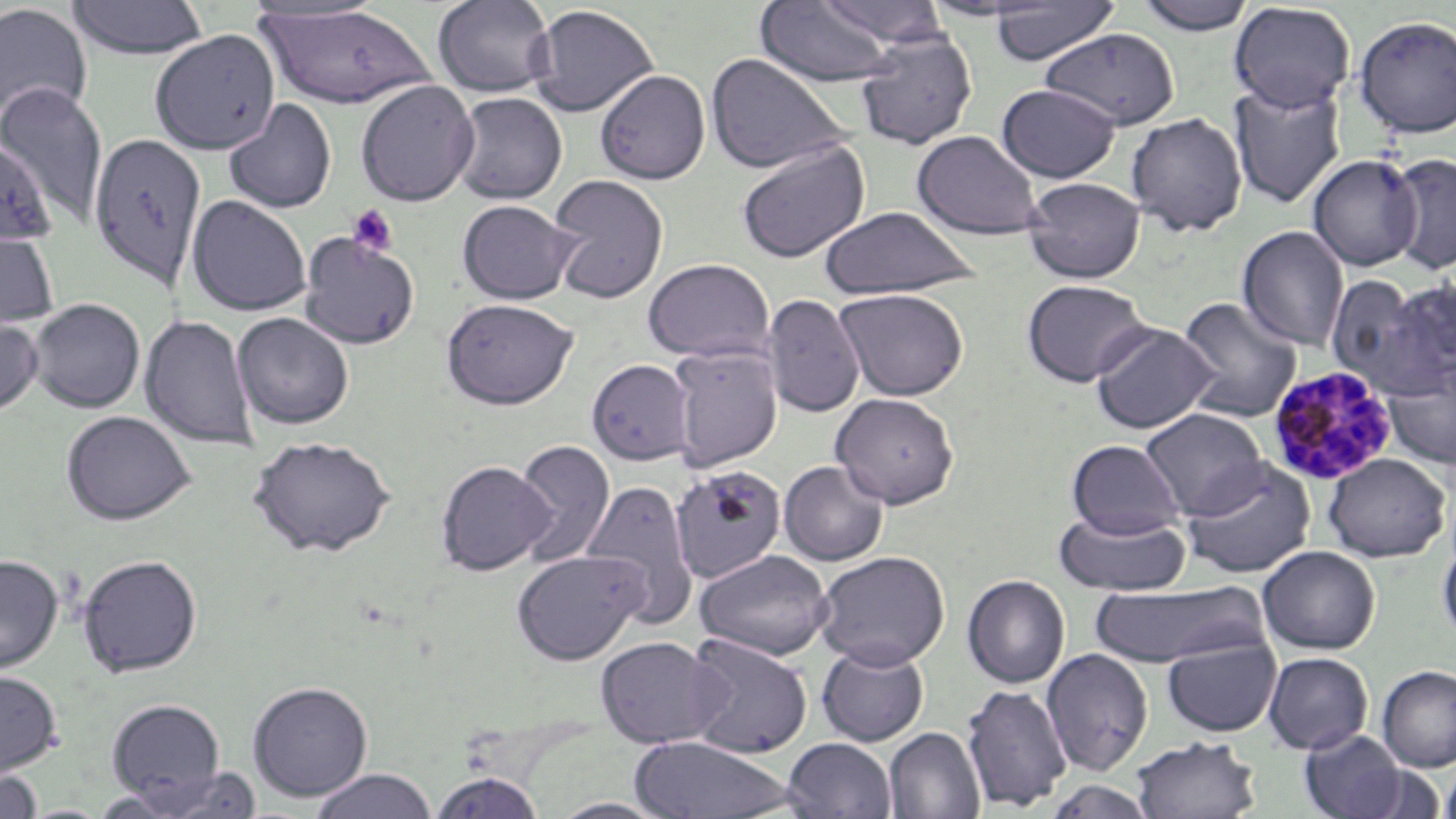

slide-level diagnosis = Plasmodium malariae
modality = light microscopy
Plasmodium malariae-infected red blood cell locations = approximate bounding boxes as (x1, y1, x2, y2) in pixels: (1268, 366, 1397, 485)
magnification = 1000x
stain = May-Grünwald-Giemsa
uninfected red blood cell locations = approximate bounding boxes as (x1, y1, x2, y2) in pixels: (67, 0, 210, 59), (432, 0, 557, 98), (818, 0, 948, 46), (1135, 0, 1259, 35), (755, 1, 897, 87), (988, 1, 1120, 65), (1229, 2, 1355, 113), (0, 3, 93, 124), (529, 4, 659, 117), (255, 5, 440, 111), (1352, 15, 1456, 139), (1040, 28, 1180, 130), (149, 30, 280, 154), (854, 30, 977, 149), (706, 52, 850, 174), (594, 69, 711, 184), (355, 80, 479, 206), (1228, 80, 1347, 209), (0, 81, 108, 226), (996, 83, 1121, 183), (450, 92, 568, 205), (224, 99, 337, 214), (1125, 112, 1248, 237), (911, 130, 1044, 240), (90, 131, 206, 294), (0, 135, 57, 246), (736, 139, 872, 264), (1388, 152, 1456, 274), (1308, 154, 1421, 270), (547, 174, 669, 304), (1022, 176, 1146, 283), (187, 195, 311, 316), (457, 199, 579, 304), (819, 206, 979, 299), (1237, 226, 1349, 351), (0, 227, 60, 332), (298, 232, 420, 348), (642, 258, 774, 363), (1326, 274, 1430, 392), (1378, 277, 1456, 393), (1021, 279, 1152, 387), (834, 288, 969, 400), (762, 294, 865, 417), (441, 297, 578, 409), (1176, 297, 1303, 423), (29, 298, 145, 413), (232, 312, 354, 429), (139, 314, 258, 450), (0, 315, 43, 418), (1091, 323, 1218, 434), (668, 347, 783, 471), (587, 359, 694, 464), (1381, 363, 1456, 470), (831, 393, 960, 507), (1140, 407, 1268, 519), (60, 410, 195, 525), (248, 434, 396, 557), (1067, 439, 1185, 538), (511, 440, 617, 565), (1323, 453, 1451, 562), (1181, 457, 1316, 578), (436, 459, 556, 575), (778, 460, 888, 565), (671, 464, 787, 582), (580, 480, 700, 628), (1054, 509, 1192, 597), (1438, 541, 1456, 644), (1258, 545, 1381, 654), (695, 549, 833, 660), (511, 550, 647, 665), (814, 550, 951, 669), (76, 553, 203, 677), (0, 554, 63, 674), (962, 575, 1070, 688), (1088, 582, 1265, 668), (682, 633, 813, 758), (1161, 635, 1281, 737), (595, 636, 723, 748), (816, 643, 930, 746), (1041, 648, 1154, 776), (1262, 651, 1373, 754), (1377, 665, 1456, 771), (0, 669, 62, 778), (247, 680, 373, 801), (961, 684, 1071, 811), (106, 698, 225, 802), (884, 727, 985, 819), (1299, 729, 1408, 819), (629, 735, 798, 819), (781, 737, 898, 819), (1131, 737, 1261, 819), (1439, 758, 1456, 819), (1356, 764, 1449, 818), (135, 766, 262, 818), (0, 768, 43, 819), (308, 768, 438, 819), (428, 770, 546, 818), (546, 797, 675, 818)
platelet locations = approximate bounding boxes as (x1, y1, x2, y2) in pixels: (346, 203, 399, 258)
preparation = thin blood film
image size = 1456×819 pixels
field of view = one of a larger specimen